Name the parasite shown.
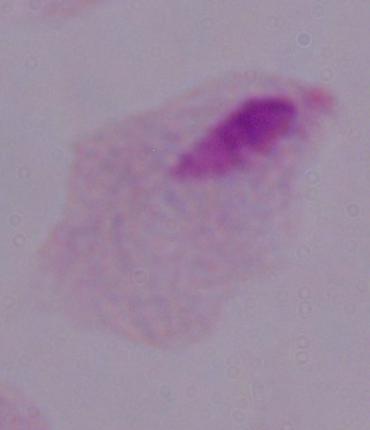
This is a trichomonad.

1000x magnification. Micrograph.